Locate every Plasmodium falciparum-infected red blood cell.
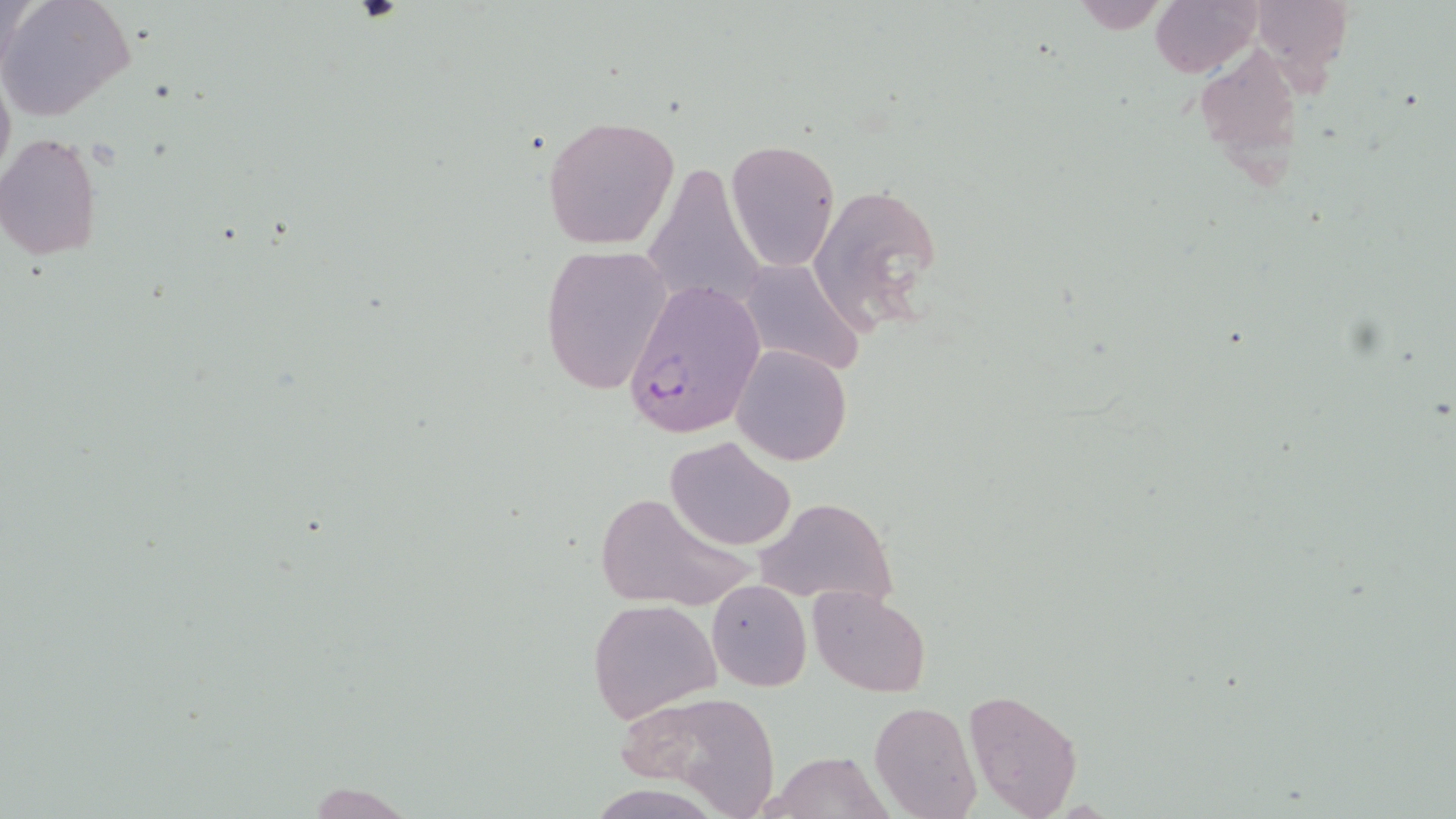

Approximate bounding boxes as named x1/y1/x2/y2 corners in pixels.
Plasmodium falciparum-infected red blood cells: (x1=621, y1=276, x2=764, y2=439).

Summary:
  - Uninfected red blood cell locations: (x1=0, y1=0, x2=137, y2=122), (x1=1150, y1=0, x2=1261, y2=77), (x1=1251, y1=0, x2=1353, y2=80), (x1=1066, y1=3, x2=1174, y2=33), (x1=1194, y1=41, x2=1301, y2=166), (x1=0, y1=63, x2=14, y2=191), (x1=541, y1=114, x2=680, y2=250), (x1=0, y1=134, x2=103, y2=261), (x1=725, y1=140, x2=840, y2=272), (x1=642, y1=165, x2=768, y2=314), (x1=806, y1=182, x2=944, y2=336), (x1=538, y1=243, x2=675, y2=396), (x1=736, y1=259, x2=866, y2=378), (x1=731, y1=344, x2=853, y2=465), (x1=666, y1=436, x2=797, y2=551), (x1=590, y1=488, x2=755, y2=612), (x1=753, y1=497, x2=899, y2=612), (x1=707, y1=580, x2=811, y2=691), (x1=806, y1=587, x2=931, y2=696), (x1=587, y1=600, x2=722, y2=722), (x1=962, y1=687, x2=1085, y2=819), (x1=618, y1=690, x2=780, y2=812), (x1=868, y1=700, x2=981, y2=819), (x1=762, y1=751, x2=891, y2=817)
  - Slide-level diagnosis: Plasmodium falciparum
  - Modality: optical microscopy
  - Magnification: 1000x
  - Preparation: thin blood smear
  - Stain: May-Grünwald-Giemsa
  - Image size: 1456×819 pixels
  - Field of view: one of a larger specimen